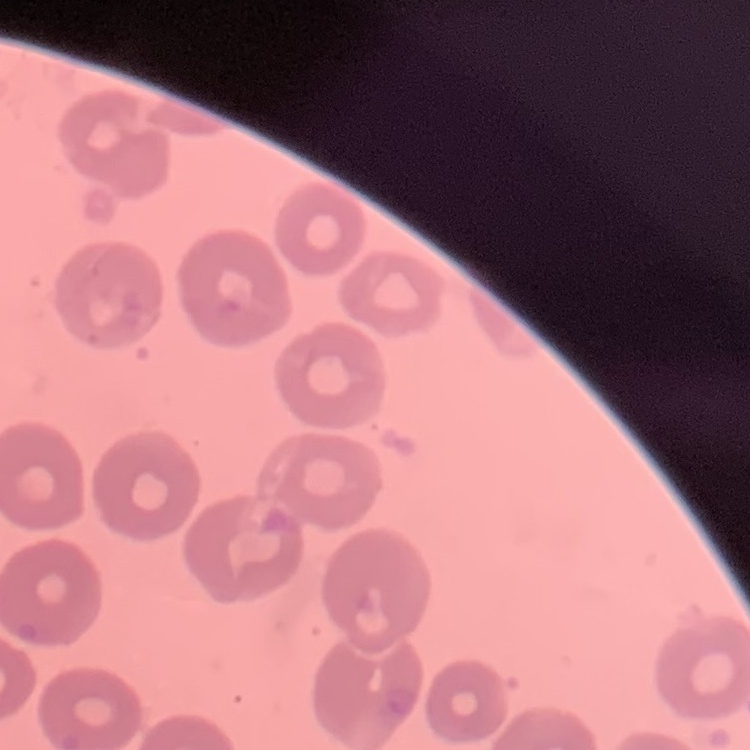
The erythrocytes exhibit no rouleaux formation. Thin blood smear. Field's or Giemsa stain. Square crop of a larger photomicrograph.